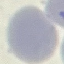 Result: no malaria parasites seen. Acquired by smartphone through the microscope eyepiece. Automatically extracted cell patch, resized to 64 × 64 pixels. Giemsa-stained preparation. Thin blood film.